Give the position of every Plasmodium parasite visible.
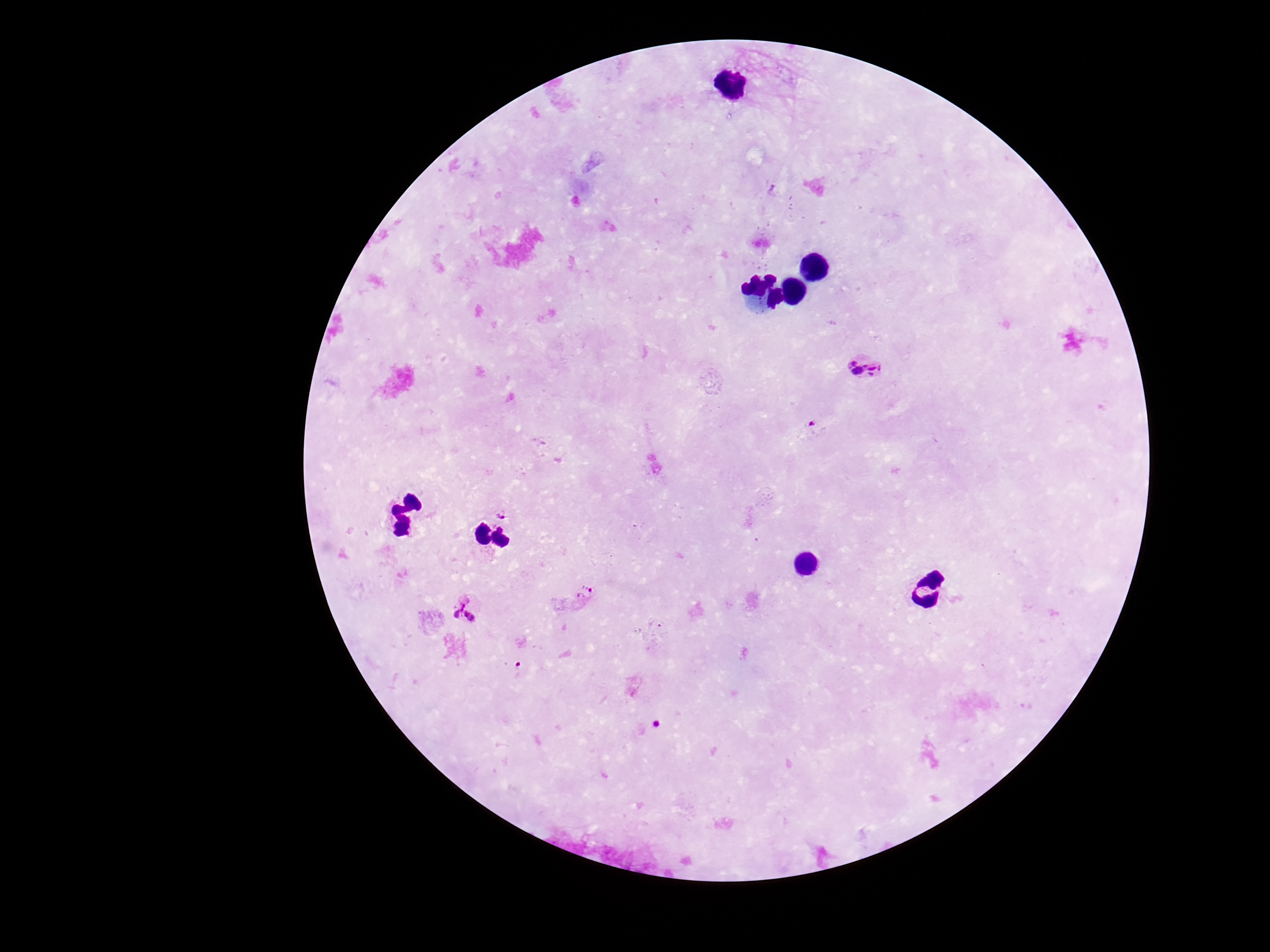
Approximate centers as [x, y] in pixels.
Plasmodium parasites: [868, 367], [813, 425], [503, 514], [585, 596], [468, 609].

Summary:
  - Field of view: one from this slide
  - Capture: smartphone camera through the microscope eyepiece
  - Patient malaria status: positive
  - Image size: 1270×952 pixels
  - Magnification: 100x
  - Preparation: thick blood smear
  - Stain: Giemsa